Assess the background quality.
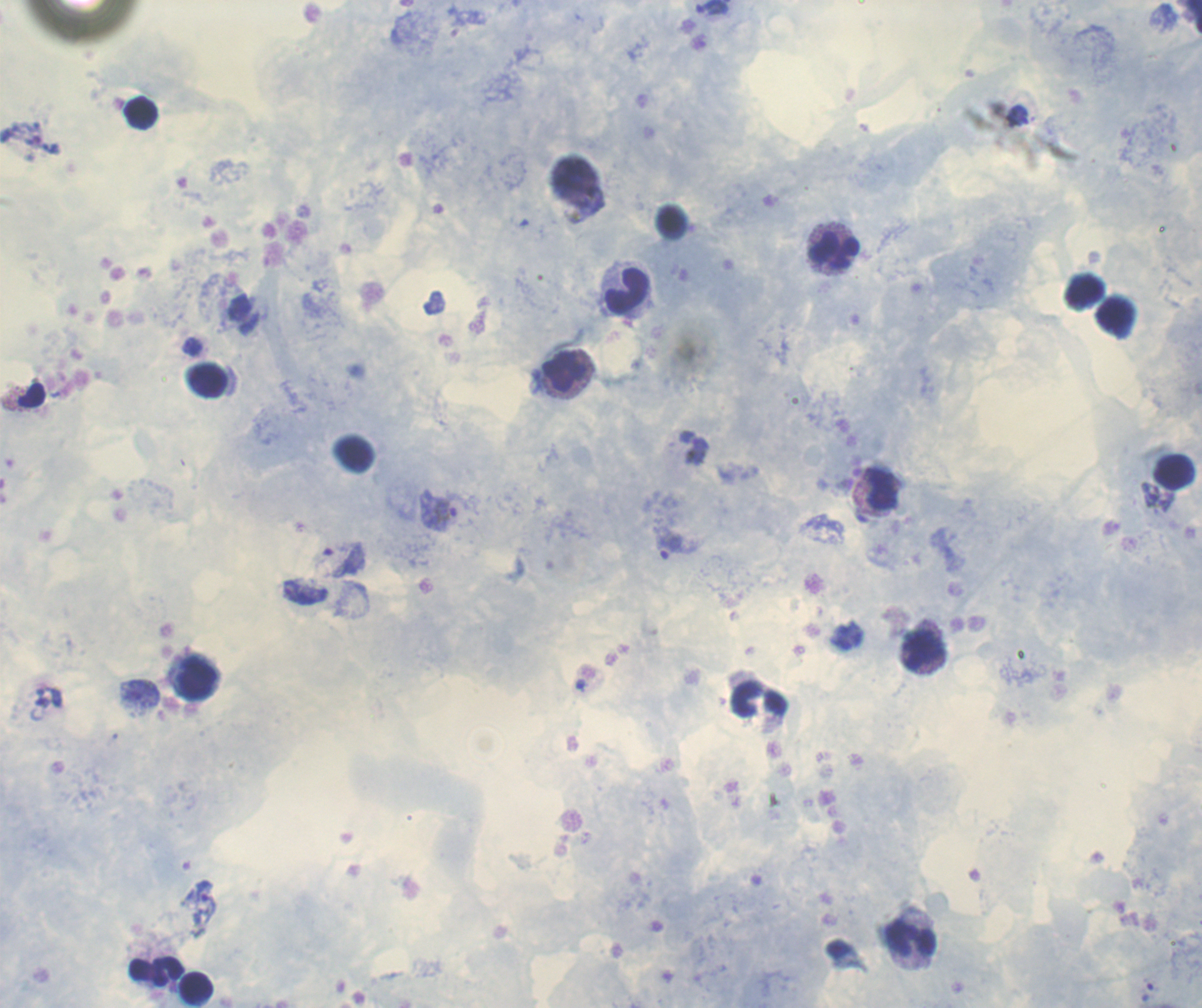
It is good.

Approximate centers as {x, y} in pixels.
Summary:
  - Leukocyte locations: {141, 114}, {673, 222}, {833, 247}, {624, 288}, {1083, 291}, {1118, 317}, {566, 372}, {207, 380}, {30, 395}, {354, 452}, {1175, 471}, {880, 489}, {847, 636}, {924, 652}, {194, 675}, {760, 701}, {912, 941}, {139, 969}, {169, 971}, {197, 988}
  - Trophozoite locations: {191, 346}, {1150, 494}, {437, 510}, {668, 544}, {304, 591}, {581, 684}, {139, 694}, {199, 906}
  - Coloration quality: good
  - Image size: 1202×1008 pixels
  - Magnification: 100x
  - Field of view: single
  - Preparation: thick smear of blood
  - Result: positive for malaria parasites
  - Context: previously used in an actual diagnosis
  - Stain: Romanowsky